Identify the cell.
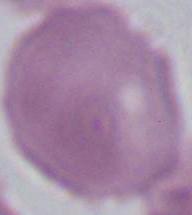
This is an erythrocyte.

Summary:
  - Magnification: 1000x
  - Modality: micrograph